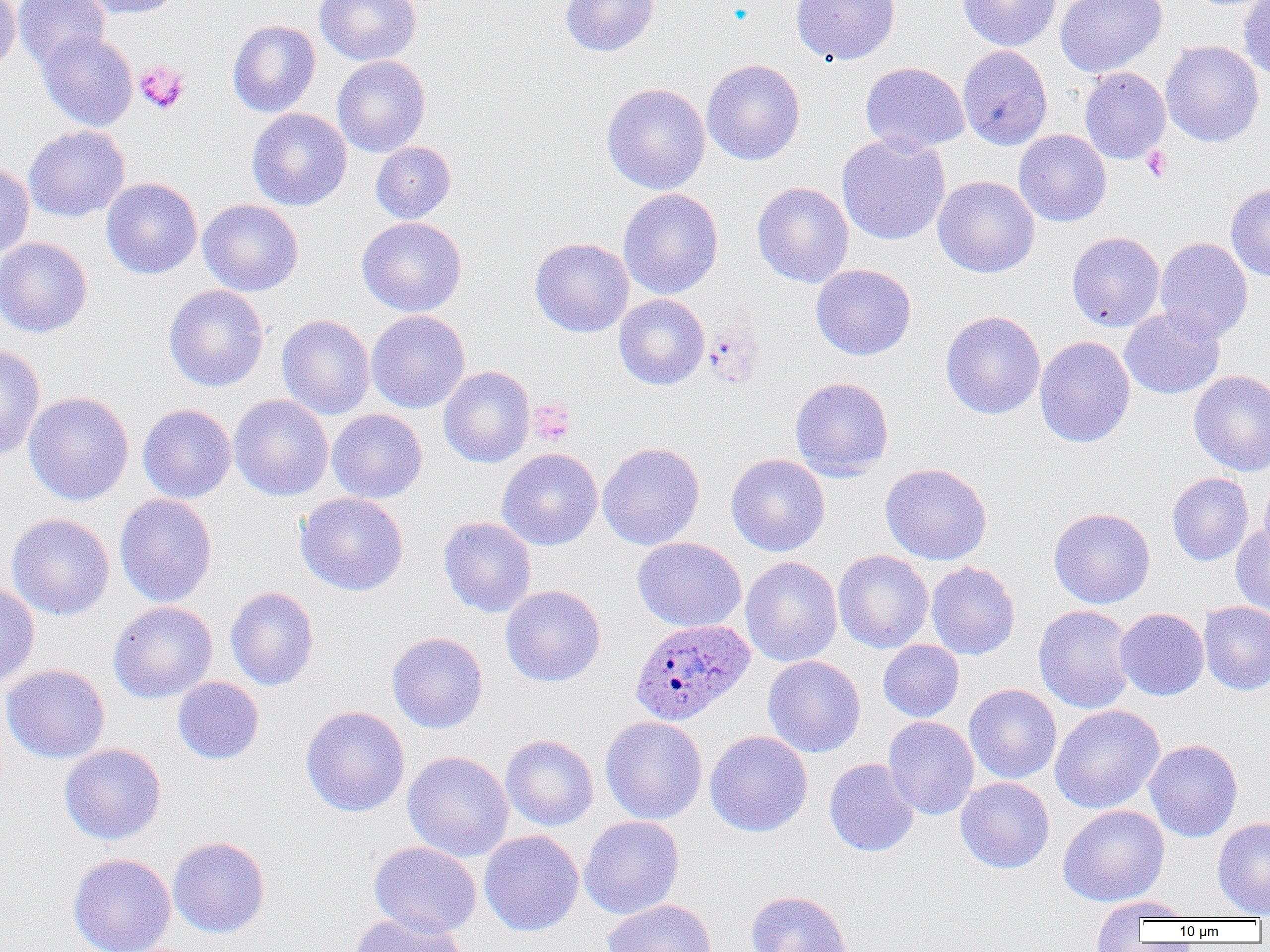

slide-level diagnosis = Plasmodium ovale
preparation = thin blood smear
platelet locations = approximate bounding boxes as [x1, y1, x2, y2] in pixels: [134, 61, 189, 114], [1141, 146, 1173, 182], [528, 398, 577, 446]
uninfected red blood cell locations = approximate bounding boxes as [x1, y1, x2, y2] in pixels: [0, 0, 20, 72], [13, 0, 110, 71], [80, 0, 183, 18], [315, 0, 422, 65], [560, 0, 659, 57], [790, 0, 900, 64], [957, 0, 1062, 51], [1055, 0, 1167, 77], [1239, 0, 1270, 83], [227, 20, 321, 117], [37, 31, 138, 131], [1160, 39, 1264, 148], [957, 44, 1053, 150], [332, 55, 431, 157], [701, 59, 805, 166], [860, 62, 969, 154], [1079, 67, 1171, 164], [601, 82, 711, 195], [247, 108, 352, 211], [23, 125, 130, 222], [1013, 129, 1112, 227], [836, 133, 951, 245], [370, 141, 456, 223], [0, 160, 35, 259], [932, 175, 1040, 278], [101, 177, 202, 280], [752, 181, 854, 288], [1225, 183, 1270, 282], [618, 188, 724, 300], [198, 199, 304, 296], [357, 216, 467, 317], [1067, 231, 1165, 332], [0, 237, 93, 339], [529, 237, 634, 337], [1155, 237, 1253, 343], [811, 263, 917, 361], [163, 284, 269, 392], [614, 294, 709, 390], [1119, 307, 1224, 399], [366, 310, 470, 413], [940, 311, 1045, 419], [276, 314, 375, 420], [1035, 336, 1136, 448], [0, 345, 45, 461], [439, 366, 535, 468], [1189, 370, 1270, 476], [790, 376, 894, 481], [23, 391, 134, 505], [229, 394, 334, 502], [137, 404, 236, 503], [327, 409, 428, 503], [597, 442, 705, 550], [496, 448, 603, 551], [726, 453, 830, 556], [880, 462, 992, 565], [1167, 472, 1254, 566], [1259, 474, 1270, 565], [295, 492, 409, 596], [114, 493, 217, 608], [1048, 507, 1155, 609], [6, 513, 115, 621], [438, 517, 537, 617], [1230, 523, 1270, 618], [632, 537, 746, 631], [833, 550, 934, 653], [740, 556, 842, 667], [926, 561, 1020, 660], [0, 581, 40, 689], [500, 585, 606, 687], [225, 586, 320, 691], [107, 601, 218, 703], [1199, 601, 1270, 695], [1034, 604, 1136, 714], [1115, 608, 1209, 700], [386, 631, 488, 733], [878, 639, 964, 722], [763, 655, 866, 758], [1, 664, 110, 763], [172, 676, 264, 765], [964, 684, 1062, 784], [1049, 704, 1165, 814], [300, 705, 410, 817], [599, 716, 708, 825], [883, 716, 979, 820], [704, 731, 813, 837], [501, 734, 599, 831], [1144, 739, 1243, 842], [59, 743, 166, 845], [402, 751, 514, 861], [824, 758, 919, 857], [955, 777, 1055, 874], [1057, 804, 1170, 907], [579, 816, 685, 919], [1212, 817, 1270, 917], [479, 830, 584, 936], [168, 836, 270, 938], [369, 841, 482, 939], [67, 853, 177, 952], [744, 890, 854, 952], [1092, 895, 1194, 934], [602, 899, 717, 952], [349, 912, 469, 952]
image size = 1270×952 pixels
magnification = 1000x
modality = light microscopy
field of view = one of a larger specimen
Plasmodium ovale-infected red blood cell locations = approximate bounding boxes as [x1, y1, x2, y2] in pixels: [629, 618, 755, 726]